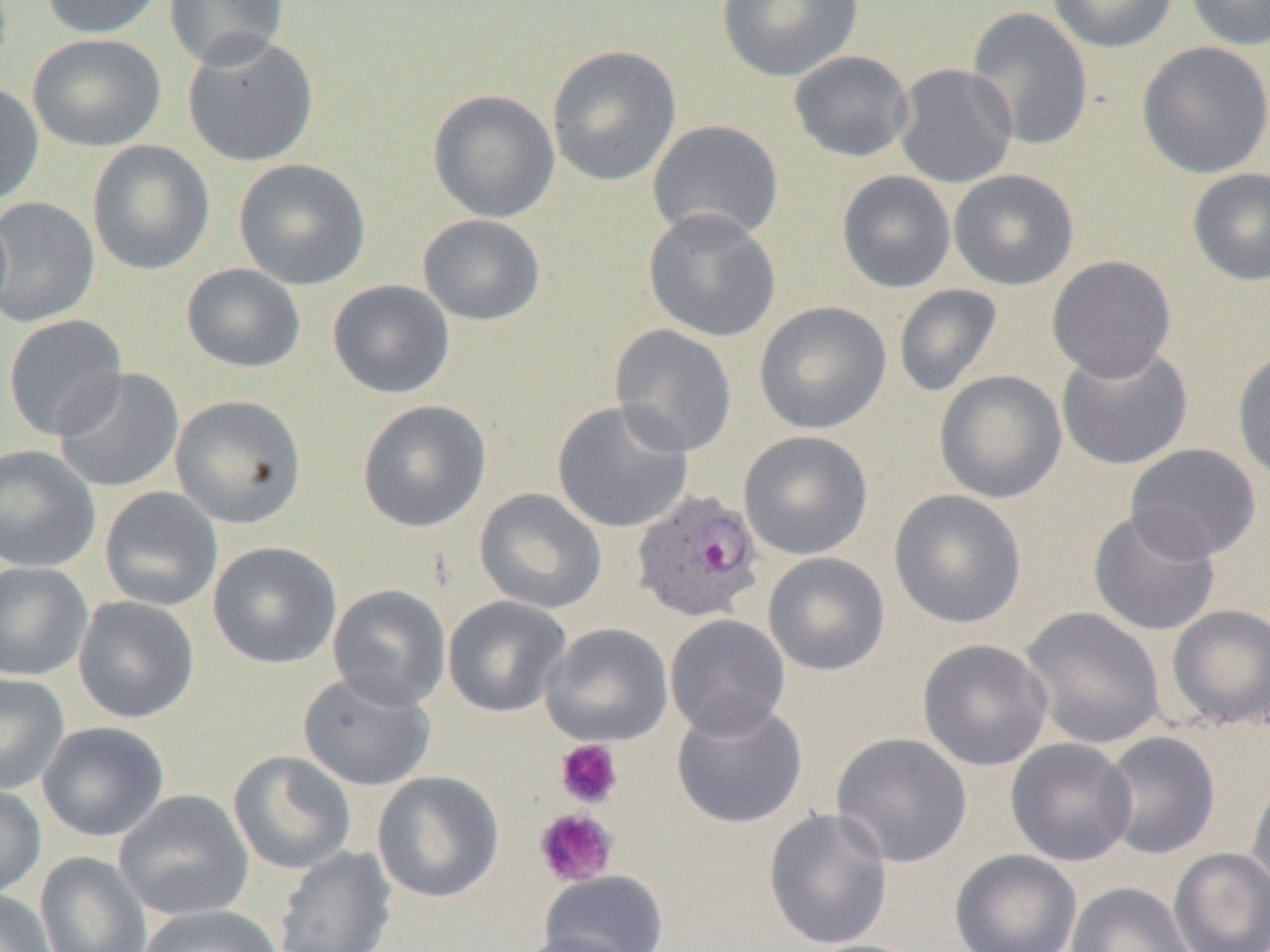
Summary:
  - Coordinate format: approximate bounding boxes as [x1, y1, x2, y2] in pixels
  - Uninfected red blood cell locations: [39, 0, 164, 39], [163, 0, 290, 69], [716, 0, 863, 83], [1047, 0, 1179, 53], [1185, 0, 1270, 51], [965, 6, 1094, 152], [27, 33, 167, 152], [182, 34, 319, 167], [1136, 41, 1270, 179], [546, 44, 682, 187], [788, 50, 915, 163], [895, 63, 1018, 188], [0, 83, 45, 207], [427, 88, 561, 223], [648, 119, 785, 243], [87, 140, 215, 276], [233, 158, 372, 290], [1187, 167, 1270, 286], [949, 169, 1079, 290], [836, 170, 956, 294], [0, 197, 100, 328], [643, 208, 781, 343], [418, 214, 546, 326], [1047, 255, 1177, 382], [181, 263, 306, 373], [327, 279, 456, 399], [894, 283, 1002, 398], [754, 300, 892, 435], [2, 314, 128, 441], [609, 324, 738, 457], [1056, 343, 1194, 471], [1232, 348, 1270, 485], [53, 367, 185, 493], [934, 369, 1068, 504], [170, 394, 307, 529], [357, 399, 492, 533], [552, 400, 694, 533], [738, 430, 873, 560], [1125, 443, 1262, 562], [0, 444, 101, 573], [99, 487, 223, 612], [474, 488, 607, 614], [889, 489, 1027, 629], [1088, 508, 1222, 637], [208, 542, 342, 669], [763, 552, 890, 677], [0, 562, 93, 681], [328, 585, 451, 710], [73, 596, 200, 724], [443, 596, 572, 718], [1166, 604, 1270, 730], [1019, 606, 1166, 750], [665, 615, 791, 737], [540, 622, 674, 747], [918, 639, 1053, 771], [298, 671, 437, 791], [0, 673, 70, 794], [671, 699, 808, 829], [37, 721, 170, 842], [1100, 731, 1221, 859], [831, 732, 973, 868], [1005, 738, 1137, 866], [228, 751, 356, 875], [372, 771, 505, 903], [1246, 774, 1270, 902], [0, 782, 47, 900], [114, 790, 254, 922], [763, 807, 893, 950], [273, 846, 397, 952], [1169, 847, 1270, 952], [949, 849, 1082, 952], [34, 851, 153, 952], [538, 870, 669, 951], [1066, 882, 1195, 952], [0, 889, 58, 952], [137, 905, 283, 952], [511, 931, 639, 952], [792, 938, 928, 952]
  - Platelet locations: [555, 739, 623, 809], [533, 808, 619, 887]
  - Plasmodium ovale-infected red blood cell locations: [631, 489, 765, 623]
  - Slide-level diagnosis: Plasmodium ovale
  - Image size: 1270×952 pixels
  - Magnification: 1000x
  - Preparation: thin blood film
  - Field of view: single
  - Modality: optical microscopy